Locate every blood parasite and identify its species.
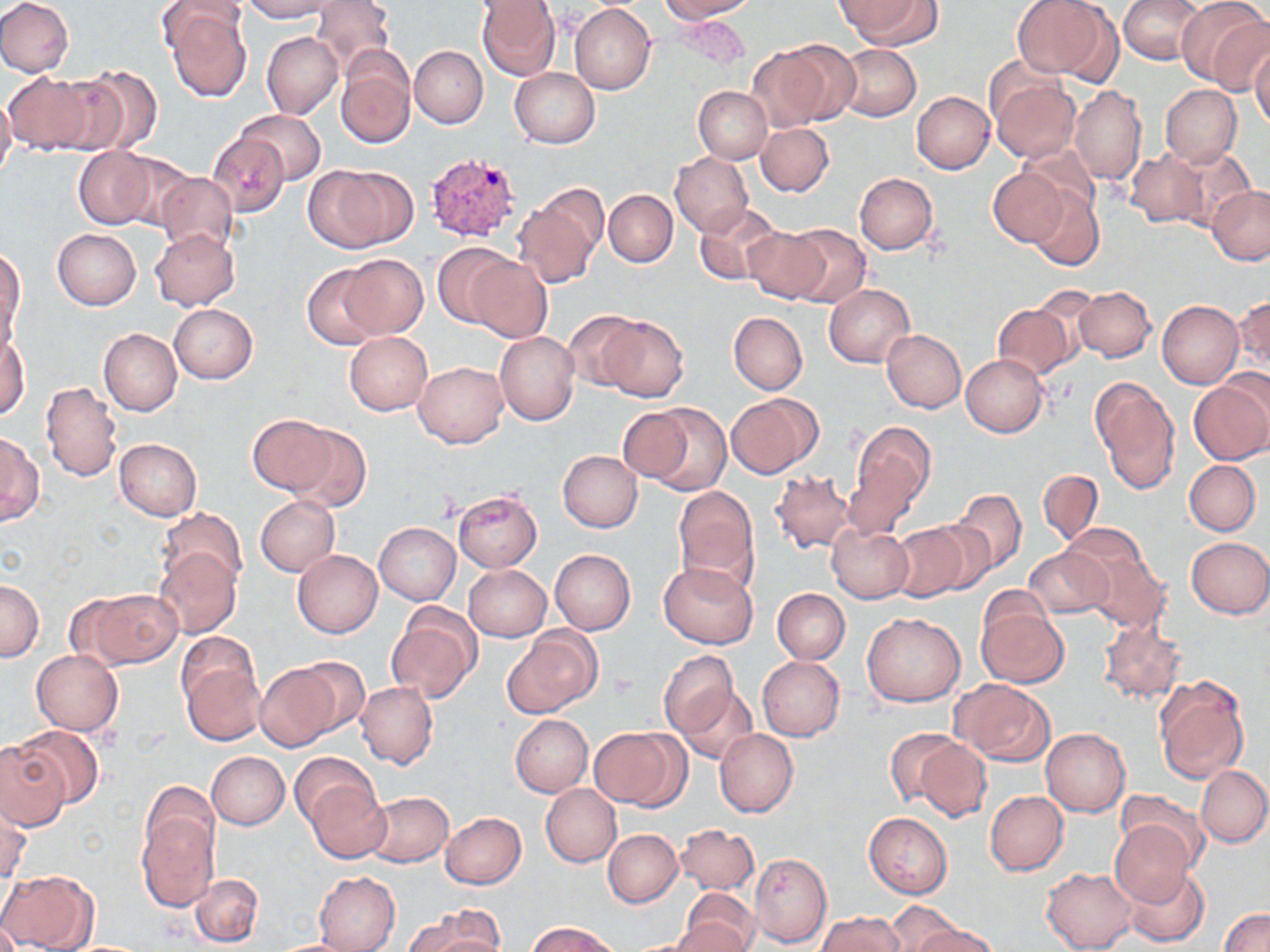
Approximate bounding boxes as named x1/y1/x2/y2 corners in pixels.
Plasmodium vivax-infected red blood cells: (x1=422, y1=152, x2=525, y2=245).
No Plasmodium falciparum, Plasmodium ovale, Plasmodium malariae, Babesia divergens, or Trypanosoma brucei observed.

Uninfected red blood cell locations: (x1=0, y1=0, x2=75, y2=77), (x1=242, y1=0, x2=336, y2=21), (x1=311, y1=0, x2=395, y2=74), (x1=659, y1=0, x2=756, y2=21), (x1=1013, y1=0, x2=1110, y2=79), (x1=1118, y1=0, x2=1203, y2=65), (x1=1175, y1=0, x2=1270, y2=91), (x1=476, y1=1, x2=561, y2=79), (x1=841, y1=1, x2=941, y2=51), (x1=570, y1=3, x2=656, y2=95), (x1=162, y1=4, x2=252, y2=103), (x1=262, y1=32, x2=343, y2=120), (x1=751, y1=42, x2=845, y2=129), (x1=837, y1=44, x2=919, y2=121), (x1=1251, y1=44, x2=1270, y2=132), (x1=410, y1=46, x2=487, y2=127), (x1=335, y1=51, x2=416, y2=149), (x1=75, y1=66, x2=164, y2=155), (x1=509, y1=67, x2=600, y2=148), (x1=4, y1=72, x2=92, y2=154), (x1=990, y1=76, x2=1080, y2=163), (x1=1161, y1=84, x2=1242, y2=166), (x1=1069, y1=85, x2=1146, y2=186), (x1=694, y1=86, x2=772, y2=163), (x1=911, y1=91, x2=996, y2=174), (x1=0, y1=94, x2=17, y2=183), (x1=237, y1=110, x2=325, y2=184), (x1=756, y1=122, x2=834, y2=197), (x1=208, y1=134, x2=288, y2=216), (x1=1017, y1=143, x2=1101, y2=223), (x1=73, y1=147, x2=157, y2=229), (x1=108, y1=150, x2=198, y2=231), (x1=1125, y1=150, x2=1208, y2=227), (x1=1162, y1=150, x2=1254, y2=233), (x1=670, y1=152, x2=752, y2=236), (x1=304, y1=164, x2=404, y2=254), (x1=990, y1=170, x2=1067, y2=247), (x1=154, y1=171, x2=238, y2=257), (x1=853, y1=172, x2=937, y2=254), (x1=1208, y1=186, x2=1270, y2=264), (x1=1027, y1=187, x2=1104, y2=271), (x1=513, y1=189, x2=605, y2=290), (x1=604, y1=190, x2=677, y2=267), (x1=694, y1=203, x2=781, y2=287), (x1=784, y1=224, x2=870, y2=309), (x1=741, y1=226, x2=827, y2=304), (x1=53, y1=228, x2=140, y2=309), (x1=150, y1=228, x2=240, y2=311), (x1=432, y1=244, x2=518, y2=328), (x1=0, y1=246, x2=26, y2=345), (x1=338, y1=254, x2=428, y2=338), (x1=465, y1=256, x2=552, y2=344), (x1=302, y1=265, x2=387, y2=350), (x1=823, y1=284, x2=914, y2=368), (x1=1074, y1=286, x2=1156, y2=362), (x1=1028, y1=287, x2=1100, y2=368), (x1=1233, y1=293, x2=1269, y2=374), (x1=1157, y1=301, x2=1244, y2=388), (x1=168, y1=303, x2=259, y2=384), (x1=992, y1=303, x2=1075, y2=380), (x1=564, y1=312, x2=642, y2=390), (x1=728, y1=312, x2=807, y2=395), (x1=597, y1=315, x2=690, y2=402), (x1=99, y1=329, x2=181, y2=416), (x1=1, y1=330, x2=30, y2=420), (x1=881, y1=330, x2=966, y2=412), (x1=495, y1=331, x2=579, y2=425), (x1=344, y1=332, x2=432, y2=414), (x1=961, y1=353, x2=1048, y2=437), (x1=414, y1=361, x2=508, y2=448), (x1=1089, y1=376, x2=1179, y2=493), (x1=1188, y1=377, x2=1270, y2=466), (x1=41, y1=382, x2=121, y2=481), (x1=725, y1=392, x2=821, y2=479), (x1=642, y1=402, x2=731, y2=497), (x1=616, y1=406, x2=700, y2=484), (x1=249, y1=415, x2=335, y2=494), (x1=842, y1=420, x2=936, y2=535), (x1=284, y1=423, x2=371, y2=512), (x1=0, y1=434, x2=42, y2=525), (x1=114, y1=438, x2=202, y2=521), (x1=558, y1=450, x2=642, y2=532), (x1=1184, y1=460, x2=1260, y2=535), (x1=1038, y1=469, x2=1104, y2=544), (x1=770, y1=470, x2=856, y2=554), (x1=673, y1=486, x2=759, y2=593), (x1=948, y1=489, x2=1025, y2=572), (x1=452, y1=490, x2=542, y2=572), (x1=255, y1=496, x2=340, y2=576), (x1=157, y1=508, x2=247, y2=593), (x1=925, y1=510, x2=1006, y2=590), (x1=374, y1=513, x2=541, y2=596), (x1=375, y1=523, x2=460, y2=604), (x1=888, y1=523, x2=973, y2=603), (x1=1061, y1=525, x2=1149, y2=591), (x1=826, y1=526, x2=913, y2=603), (x1=1185, y1=536, x2=1270, y2=618), (x1=1024, y1=546, x2=1112, y2=619), (x1=155, y1=550, x2=242, y2=637), (x1=292, y1=550, x2=383, y2=638), (x1=549, y1=550, x2=635, y2=635), (x1=1084, y1=550, x2=1171, y2=633), (x1=657, y1=563, x2=759, y2=649), (x1=464, y1=564, x2=552, y2=640), (x1=0, y1=580, x2=44, y2=662), (x1=773, y1=588, x2=849, y2=663), (x1=80, y1=589, x2=182, y2=669), (x1=977, y1=602, x2=1069, y2=688), (x1=386, y1=604, x2=480, y2=702), (x1=862, y1=612, x2=965, y2=707), (x1=1099, y1=617, x2=1188, y2=707), (x1=506, y1=626, x2=600, y2=718), (x1=176, y1=631, x2=260, y2=710), (x1=658, y1=649, x2=740, y2=739), (x1=31, y1=651, x2=122, y2=736), (x1=287, y1=656, x2=370, y2=738), (x1=757, y1=656, x2=844, y2=740), (x1=181, y1=663, x2=266, y2=747), (x1=254, y1=663, x2=340, y2=751), (x1=1154, y1=675, x2=1249, y2=784), (x1=952, y1=679, x2=1056, y2=766), (x1=357, y1=683, x2=438, y2=769), (x1=675, y1=683, x2=758, y2=765), (x1=510, y1=715, x2=592, y2=796), (x1=13, y1=724, x2=105, y2=811), (x1=589, y1=726, x2=686, y2=808), (x1=886, y1=726, x2=972, y2=813), (x1=1041, y1=728, x2=1130, y2=816), (x1=715, y1=729, x2=798, y2=816), (x1=916, y1=739, x2=990, y2=823), (x1=0, y1=741, x2=69, y2=828), (x1=206, y1=751, x2=289, y2=829), (x1=290, y1=753, x2=376, y2=830), (x1=1197, y1=765, x2=1270, y2=846), (x1=140, y1=782, x2=219, y2=865), (x1=305, y1=783, x2=389, y2=863), (x1=541, y1=783, x2=621, y2=867), (x1=364, y1=790, x2=453, y2=867), (x1=985, y1=790, x2=1068, y2=875), (x1=1117, y1=790, x2=1208, y2=870), (x1=1, y1=798, x2=31, y2=882), (x1=137, y1=807, x2=218, y2=911), (x1=439, y1=812, x2=526, y2=888), (x1=865, y1=813, x2=952, y2=898), (x1=1109, y1=818, x2=1196, y2=907), (x1=676, y1=824, x2=758, y2=895), (x1=603, y1=829, x2=683, y2=907), (x1=749, y1=852, x2=832, y2=946), (x1=1042, y1=867, x2=1137, y2=951), (x1=1122, y1=867, x2=1209, y2=947), (x1=0, y1=870, x2=98, y2=952), (x1=314, y1=871, x2=400, y2=952), (x1=189, y1=873, x2=262, y2=947), (x1=679, y1=891, x2=760, y2=951), (x1=882, y1=903, x2=960, y2=951), (x1=406, y1=907, x2=499, y2=951), (x1=1220, y1=908, x2=1270, y2=952), (x1=818, y1=912, x2=906, y2=952), (x1=671, y1=919, x2=750, y2=952), (x1=528, y1=922, x2=616, y2=952), (x1=912, y1=924, x2=998, y2=952), (x1=266, y1=938, x2=369, y2=951). Platelet locations: (x1=607, y1=671, x2=636, y2=699). Slide-level diagnosis: Plasmodium vivax. Image is 1270×952 pixels. Optical microscopy. Thin blood smear. Single field of view. May-Grünwald-Giemsa stain. 1000x magnification.